Assess this cell for malaria.
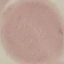
Uninfected.

image type = cell patch, automatically extracted from a larger field of view and resized to 64 × 64 pixels
preparation = thin blood film
stain = Giemsa
capture = smartphone through the microscope eyepiece